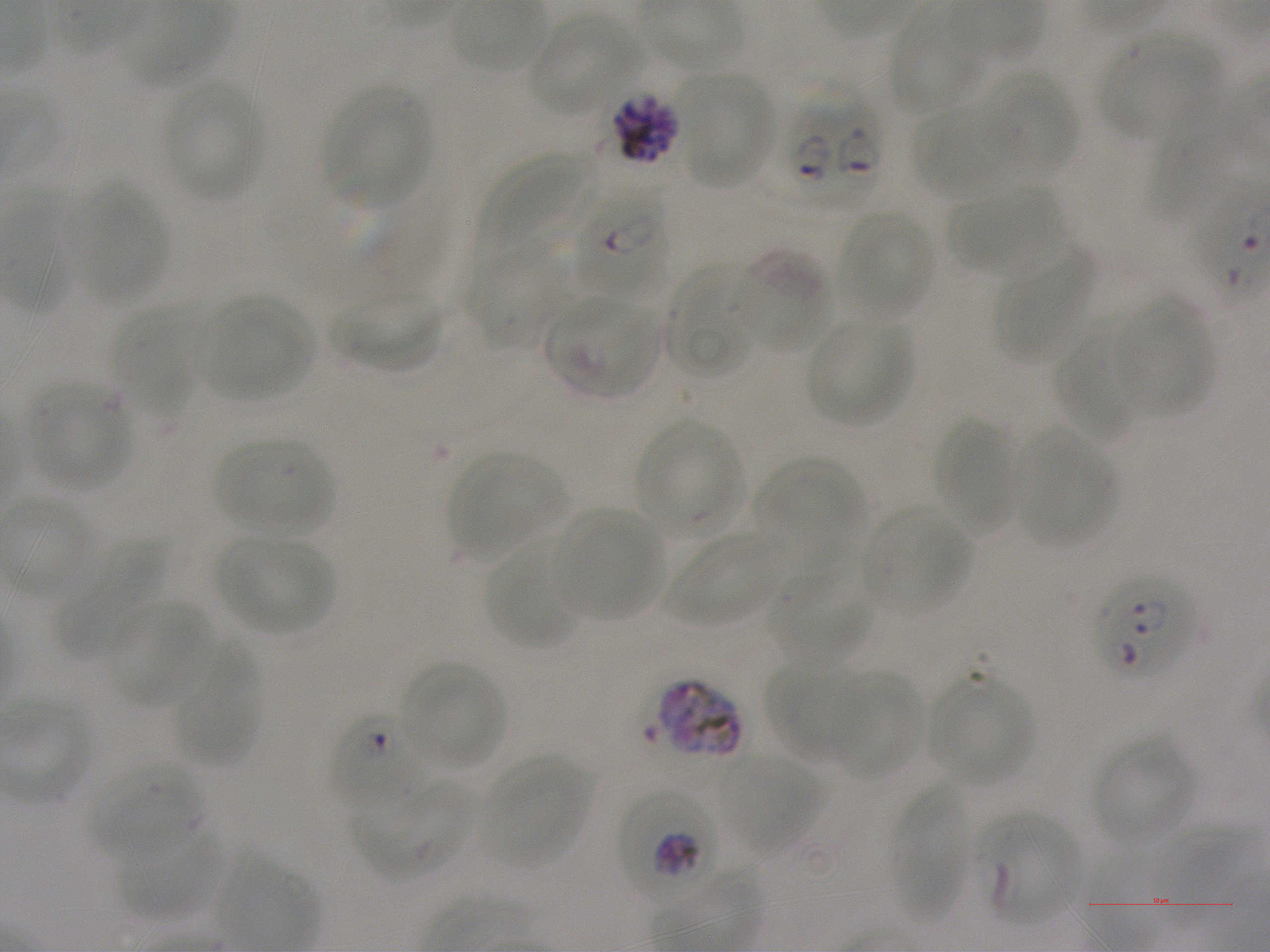
Not every red blood cell is marked. A life-cycle stage — or a range of stages, where the recorded stages span more than one — follows each staged infected red blood cell.
culture = in-vitro Plasmodium falciparum strain NF54, static
field of view = single
preparation = thin blood smear
stain = Giemsa
donor blood group = A+
life-cycle stages observed = trophozoite, schizont
objective = 100x, oil immersion, numerical aperture 1.25
locations of uninfected red blood cells = approximate bounding boxes as {x1, y1, x2, y2} in pixels: {890, 10, 983, 116}, {529, 14, 649, 114}, {1099, 34, 1222, 143}, {976, 71, 1078, 180}, {678, 74, 773, 187}, {162, 83, 264, 200}, {324, 84, 430, 208}, {1149, 86, 1236, 222}, {911, 104, 1016, 201}, {480, 151, 598, 267}, {79, 183, 168, 308}, {948, 185, 1067, 279}, {839, 210, 936, 320}, {465, 243, 569, 350}, {736, 250, 832, 353}, {996, 253, 1093, 365}, {664, 260, 762, 377}, {332, 290, 444, 372}, {201, 294, 314, 401}, {1115, 297, 1216, 416}, {111, 306, 198, 419}, {805, 318, 912, 427}, {1055, 320, 1142, 439}, {30, 383, 131, 490}, {932, 416, 1016, 536}, {636, 419, 745, 539}, {1016, 431, 1115, 546}, {215, 437, 336, 536}, {447, 451, 565, 560}, {754, 456, 864, 559}, {863, 505, 972, 616}, {555, 506, 664, 622}, {667, 533, 785, 627}, {216, 536, 330, 636}, {55, 539, 165, 658}, {485, 539, 581, 650}, {768, 562, 874, 668}, {106, 600, 213, 710}, {173, 642, 262, 768}, {398, 661, 505, 771}, {765, 664, 863, 761}, {826, 671, 923, 779}, {928, 673, 1034, 786}, {1092, 737, 1196, 849}, {715, 753, 834, 858}, {479, 755, 592, 869}, {88, 759, 206, 864}, {354, 777, 473, 880}, {889, 782, 971, 919}, {1151, 822, 1247, 929}, {119, 826, 218, 919}
locations of red blood cells of indeterminate infection status = approximate bounding boxes as {x1, y1, x2, y2} in pixels: {544, 297, 658, 398}, {649, 678, 744, 763}, {981, 815, 1081, 925}
locations of infected red blood cells = approximate bounding boxes as {x1, y1, x2, y2} in pixels: {774, 85, 882, 210}; {610, 92, 682, 166} late schizont; {572, 184, 669, 301} early ring to early trophozoite; {1093, 574, 1197, 681}; {332, 713, 427, 808}; {617, 788, 719, 905} trophozoite
image size = 1270×952 pixels